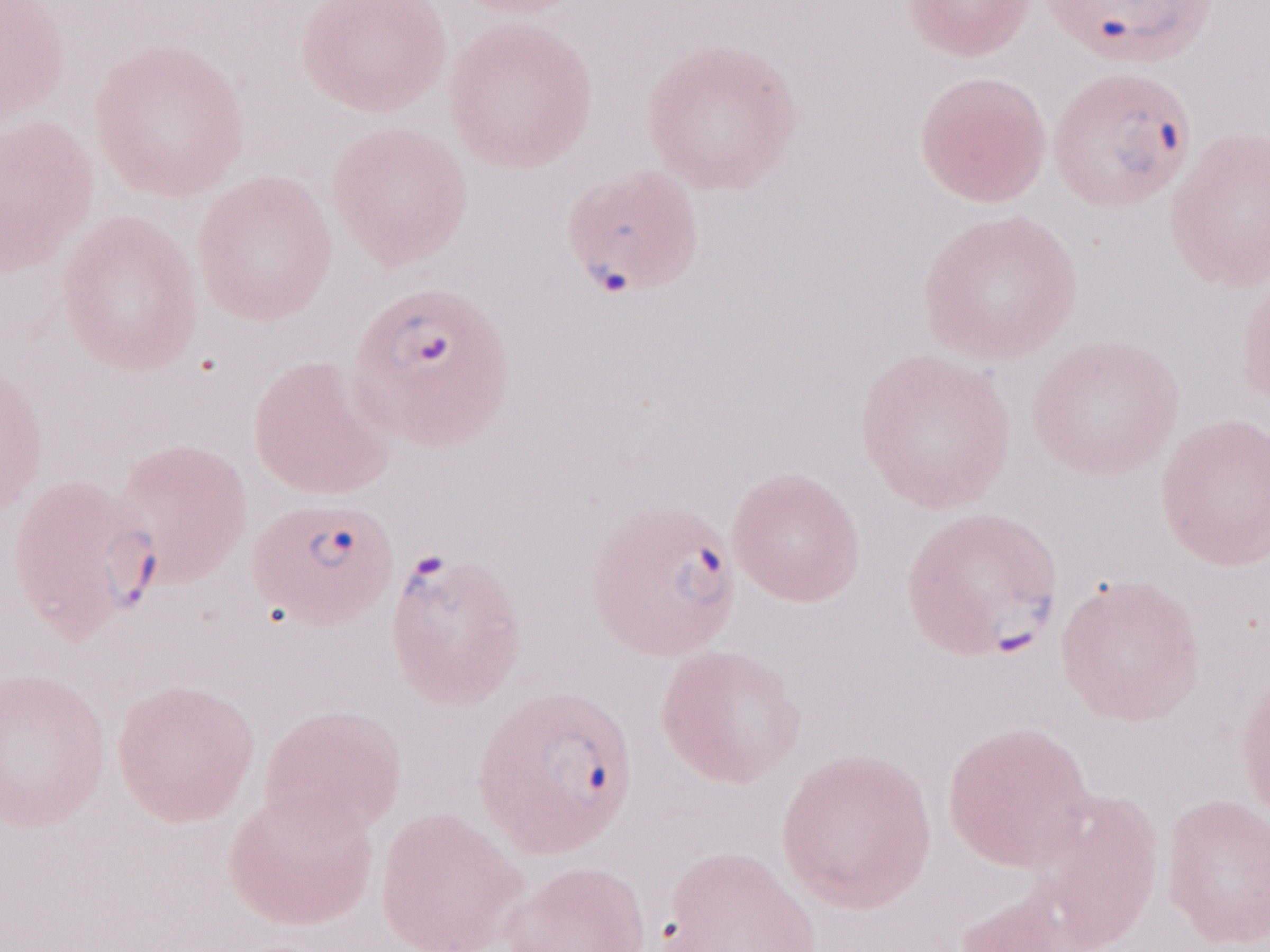 Single field of view. Magnification: 1,000x. Thin peripheral-blood smear. Olympus BX43 microscope, Olympus DP73 camera. Image is 1270×952 pixels. May-Grünwald-Giemsa-stained preparation. Malaria diagnosis (patient-level): positive.